State which parasite is depicted.
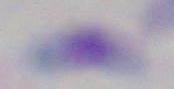
Toxoplasma gondii.

Captured at 1000x magnification. Micrograph.